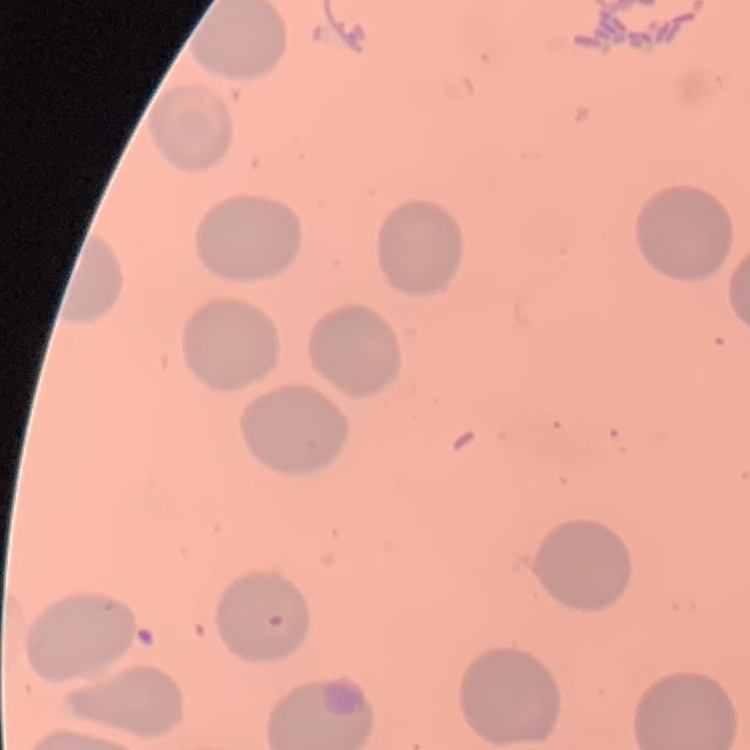
{
  "red_blood_cell_morphology": "no rouleaux formation",
  "stain": "Field's or Giemsa",
  "image_type": "square crop of a larger photomicrograph",
  "preparation": "thin peripheral smear"
}